Classify this cell by malaria status.
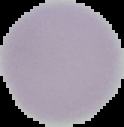

Uninfected.

From a thin blood film. Image is 124×127 pixels. Cell region segmented out of the field of view; the surrounding area is masked to black.